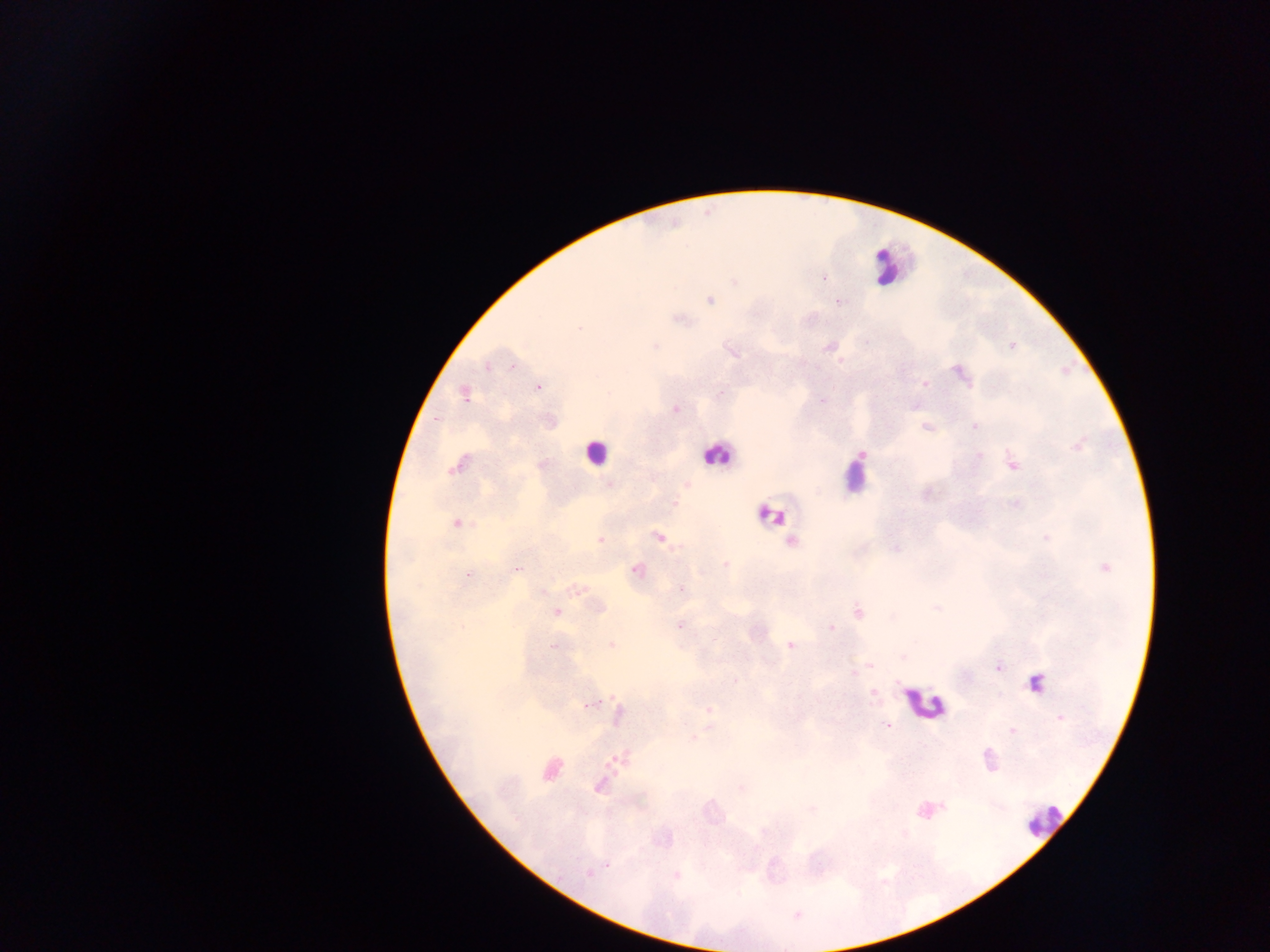

Approximate centers as {x, y} in pixels. Malaria parasite locations: {823, 278}, {734, 282}, {709, 299}, {839, 301}, {680, 319}, {579, 328}, {654, 345}, {1011, 345}, {828, 346}, {487, 367}, {960, 373}, {924, 384}, {538, 386}, {464, 394}, {821, 400}, {675, 408}, {926, 426}, {973, 426}, {1077, 445}, {977, 456}, {458, 463}, {1012, 463}, {541, 465}, {609, 484}, {687, 484}, {673, 503}, {1016, 504}, {456, 523}, {658, 537}, {600, 540}, {792, 541}, {725, 565}, {1104, 567}, {517, 568}, {636, 569}, {468, 575}, {577, 589}, {681, 589}, {598, 608}, {556, 611}, {857, 612}, {679, 625}, {830, 628}, {611, 645}, {789, 645}, {553, 646}, {869, 664}, {997, 667}, {852, 673}, {733, 679}, {1035, 683}, {873, 693}, {591, 703}, {708, 710}, {619, 715}, {1059, 718}, {887, 725}, {1012, 731}, {693, 738}, {621, 758}, {988, 759}, {549, 768}, {599, 784}, {741, 788}, {812, 807}, {607, 863}, {588, 873}, {676, 876}. Leukocyte locations: {888, 266}, {596, 451}, {717, 455}, {854, 474}, {770, 514}, {925, 704}, {1042, 820}. Image is 1270×952 pixels. Mobile-phone photograph taken through the microscope. Collected in Ghana. One field of view. Thick blood smear.